Locate platelets.
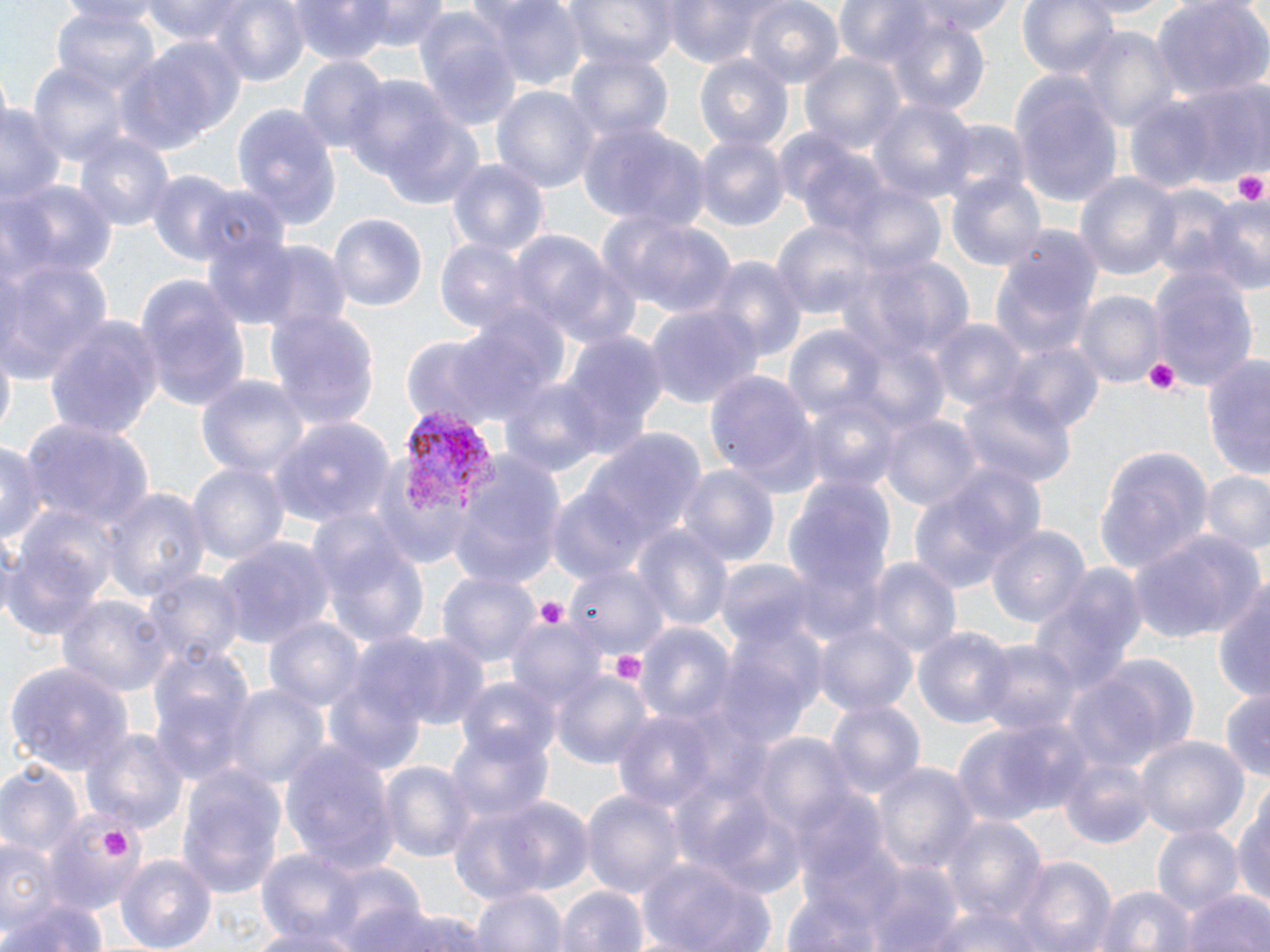
Approximate bounding boxes as named x1/y1/x2/y2 corners in pixels.
Platelets: (x1=1230, y1=169, x2=1269, y2=207), (x1=1142, y1=357, x2=1183, y2=396), (x1=534, y1=597, x2=567, y2=631), (x1=605, y1=648, x2=650, y2=692), (x1=100, y1=825, x2=132, y2=860).

Summary:
  - Plasmodium vivax-infected red blood cell locations: (x1=402, y1=410, x2=497, y2=519)
  - Uninfected red blood cell locations: (x1=138, y1=0, x2=256, y2=46), (x1=207, y1=0, x2=313, y2=90), (x1=289, y1=0, x2=394, y2=65), (x1=363, y1=0, x2=449, y2=52), (x1=482, y1=0, x2=587, y2=90), (x1=563, y1=0, x2=678, y2=71), (x1=659, y1=0, x2=780, y2=66), (x1=909, y1=0, x2=1015, y2=37), (x1=1018, y1=0, x2=1122, y2=82), (x1=1153, y1=0, x2=1270, y2=99), (x1=743, y1=1, x2=845, y2=89), (x1=52, y1=5, x2=162, y2=99), (x1=410, y1=11, x2=522, y2=134), (x1=879, y1=16, x2=993, y2=115), (x1=1075, y1=28, x2=1180, y2=131), (x1=120, y1=35, x2=245, y2=153), (x1=565, y1=49, x2=675, y2=144), (x1=801, y1=51, x2=906, y2=156), (x1=693, y1=53, x2=794, y2=156), (x1=297, y1=57, x2=388, y2=157), (x1=25, y1=61, x2=131, y2=165), (x1=343, y1=74, x2=468, y2=189), (x1=1010, y1=77, x2=1122, y2=205), (x1=1170, y1=82, x2=1268, y2=184), (x1=493, y1=84, x2=600, y2=198), (x1=870, y1=99, x2=977, y2=207), (x1=0, y1=101, x2=62, y2=206), (x1=233, y1=103, x2=343, y2=228), (x1=376, y1=115, x2=486, y2=208), (x1=936, y1=118, x2=1030, y2=205), (x1=577, y1=120, x2=705, y2=228), (x1=73, y1=133, x2=176, y2=235), (x1=694, y1=135, x2=787, y2=233), (x1=447, y1=159, x2=549, y2=258), (x1=145, y1=170, x2=245, y2=265), (x1=946, y1=171, x2=1046, y2=274), (x1=1074, y1=171, x2=1182, y2=282), (x1=2, y1=180, x2=119, y2=286), (x1=1146, y1=180, x2=1236, y2=283), (x1=845, y1=186, x2=947, y2=278), (x1=1201, y1=193, x2=1270, y2=294), (x1=328, y1=213, x2=429, y2=318), (x1=601, y1=213, x2=737, y2=318), (x1=770, y1=219, x2=879, y2=320), (x1=985, y1=229, x2=1104, y2=365), (x1=200, y1=231, x2=302, y2=328), (x1=508, y1=233, x2=616, y2=336), (x1=434, y1=235, x2=539, y2=333), (x1=248, y1=240, x2=352, y2=336), (x1=847, y1=251, x2=977, y2=364), (x1=545, y1=257, x2=646, y2=353), (x1=703, y1=257, x2=807, y2=368), (x1=0, y1=258, x2=112, y2=382), (x1=1149, y1=266, x2=1261, y2=392), (x1=132, y1=272, x2=253, y2=417), (x1=1074, y1=292, x2=1165, y2=390), (x1=646, y1=303, x2=760, y2=411), (x1=265, y1=308, x2=380, y2=429), (x1=43, y1=314, x2=167, y2=441), (x1=929, y1=318, x2=1028, y2=414), (x1=783, y1=326, x2=886, y2=428), (x1=397, y1=329, x2=534, y2=431), (x1=558, y1=331, x2=666, y2=459), (x1=1003, y1=343, x2=1102, y2=437), (x1=1204, y1=351, x2=1270, y2=481), (x1=704, y1=368, x2=823, y2=490), (x1=196, y1=371, x2=310, y2=481), (x1=501, y1=376, x2=605, y2=478), (x1=959, y1=384, x2=1077, y2=493), (x1=800, y1=389, x2=904, y2=495), (x1=880, y1=412, x2=981, y2=513), (x1=23, y1=419, x2=154, y2=533), (x1=270, y1=419, x2=394, y2=526), (x1=581, y1=429, x2=704, y2=560), (x1=2, y1=441, x2=45, y2=552), (x1=1093, y1=446, x2=1212, y2=578), (x1=445, y1=449, x2=567, y2=587), (x1=364, y1=454, x2=470, y2=570), (x1=186, y1=459, x2=290, y2=571), (x1=675, y1=465, x2=780, y2=570), (x1=910, y1=468, x2=1036, y2=593), (x1=1199, y1=471, x2=1270, y2=555), (x1=785, y1=475, x2=895, y2=599), (x1=101, y1=485, x2=209, y2=602), (x1=544, y1=486, x2=652, y2=588), (x1=985, y1=522, x2=1091, y2=630), (x1=636, y1=527, x2=734, y2=636), (x1=1134, y1=530, x2=1265, y2=645), (x1=320, y1=536, x2=433, y2=649), (x1=217, y1=538, x2=334, y2=652), (x1=2, y1=544, x2=108, y2=644), (x1=868, y1=558, x2=961, y2=663), (x1=714, y1=559, x2=820, y2=646), (x1=1028, y1=562, x2=1146, y2=700), (x1=565, y1=563, x2=669, y2=655), (x1=141, y1=567, x2=246, y2=666), (x1=438, y1=568, x2=541, y2=669), (x1=1214, y1=580, x2=1270, y2=707), (x1=61, y1=596, x2=173, y2=701), (x1=264, y1=615, x2=366, y2=713), (x1=507, y1=616, x2=609, y2=712), (x1=718, y1=618, x2=825, y2=746), (x1=815, y1=621, x2=917, y2=717), (x1=638, y1=622, x2=736, y2=726), (x1=916, y1=625, x2=1016, y2=733), (x1=388, y1=633, x2=493, y2=731), (x1=974, y1=638, x2=1079, y2=738), (x1=149, y1=648, x2=252, y2=780), (x1=1064, y1=656, x2=1195, y2=773), (x1=6, y1=662, x2=133, y2=775), (x1=552, y1=669, x2=649, y2=769), (x1=457, y1=677, x2=561, y2=767), (x1=225, y1=682, x2=330, y2=792), (x1=1220, y1=688, x2=1270, y2=781), (x1=826, y1=700, x2=924, y2=801), (x1=612, y1=710, x2=722, y2=811), (x1=953, y1=716, x2=1090, y2=826), (x1=446, y1=724, x2=552, y2=828), (x1=82, y1=726, x2=187, y2=838), (x1=1135, y1=734, x2=1249, y2=841), (x1=752, y1=735, x2=855, y2=838), (x1=283, y1=741, x2=397, y2=874), (x1=1057, y1=754, x2=1156, y2=850), (x1=374, y1=757, x2=477, y2=867), (x1=0, y1=759, x2=83, y2=864), (x1=873, y1=761, x2=980, y2=878), (x1=174, y1=764, x2=286, y2=903), (x1=1232, y1=787, x2=1270, y2=918), (x1=580, y1=788, x2=687, y2=899), (x1=454, y1=793, x2=595, y2=900), (x1=37, y1=811, x2=143, y2=939), (x1=941, y1=815, x2=1047, y2=928), (x1=1152, y1=823, x2=1244, y2=919), (x1=1, y1=834, x2=53, y2=932), (x1=255, y1=849, x2=367, y2=946), (x1=116, y1=854, x2=217, y2=952), (x1=635, y1=857, x2=780, y2=952), (x1=1010, y1=857, x2=1116, y2=951), (x1=320, y1=860, x2=426, y2=948), (x1=862, y1=861, x2=965, y2=952), (x1=554, y1=884, x2=650, y2=952), (x1=1094, y1=884, x2=1196, y2=952), (x1=469, y1=885, x2=567, y2=952), (x1=1182, y1=887, x2=1270, y2=952), (x1=1, y1=897, x2=110, y2=952), (x1=922, y1=901, x2=1053, y2=952), (x1=358, y1=904, x2=493, y2=952), (x1=249, y1=924, x2=368, y2=952)
  - Slide-level diagnosis: Plasmodium vivax
  - Preparation: thin blood film
  - Image size: 1270×952 pixels
  - Modality: light microscopy
  - Field of view: single
  - Magnification: 1000x
  - Stain: May-Grünwald-Giemsa